Give the position of every Plasmodium parasite visible.
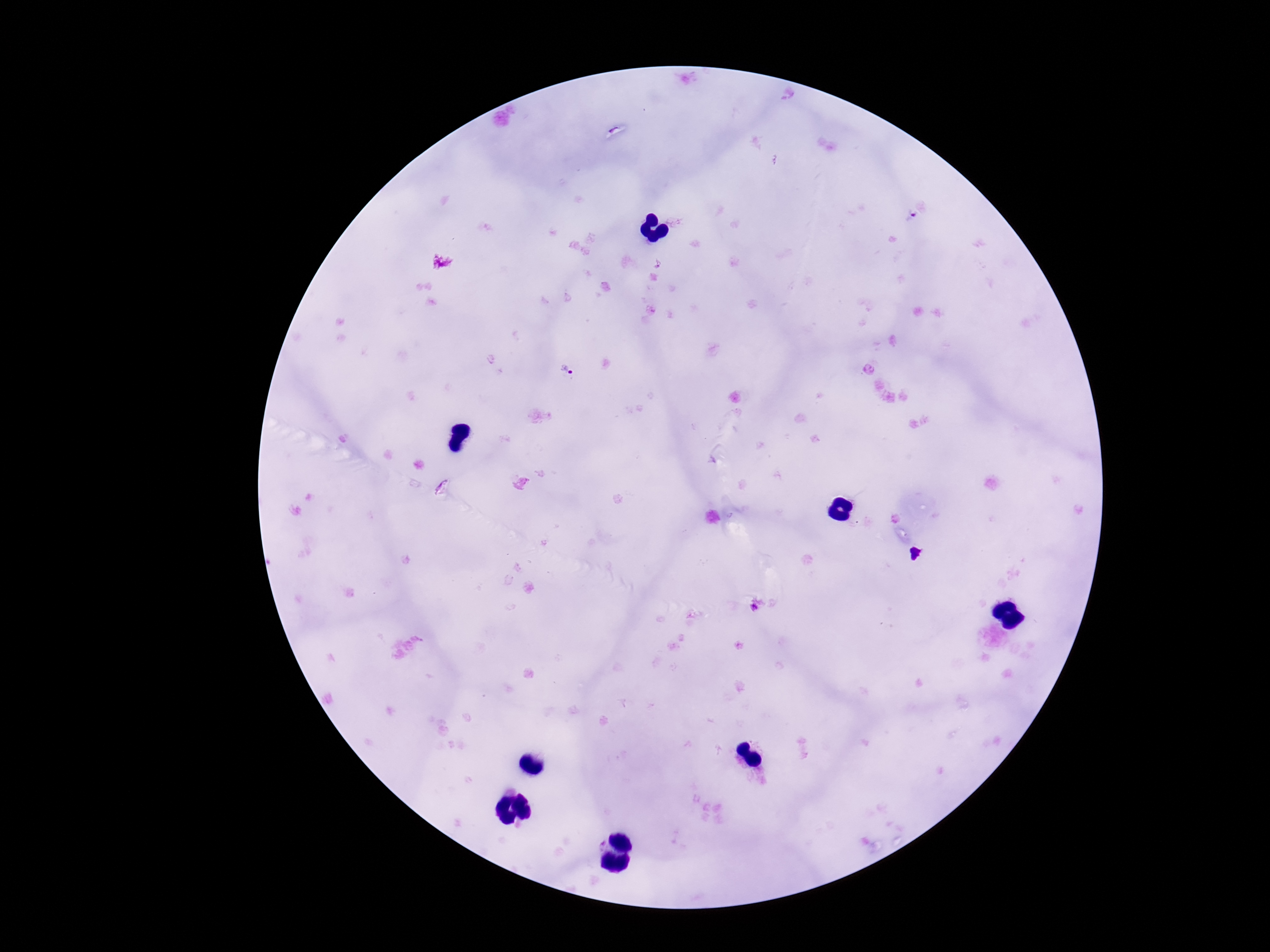

Approximate centers as {x, y} in pixels.
Plasmodium parasites: {566, 370}, {756, 607}.

preparation = thick peripheral-blood smear
magnification = 100x
patient malaria status = infected
capture = smartphone camera through the microscope eyepiece
stain = Giemsa
image size = 1270×952 pixels
field of view = one from this slide